Report the malaria status of this cell.
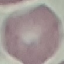

It is uninfected.

stain = Giemsa
preparation = thin blood smear
capture = smartphone through the microscope eyepiece
image type = automatically extracted cell patch, resized to 64 × 64 pixels